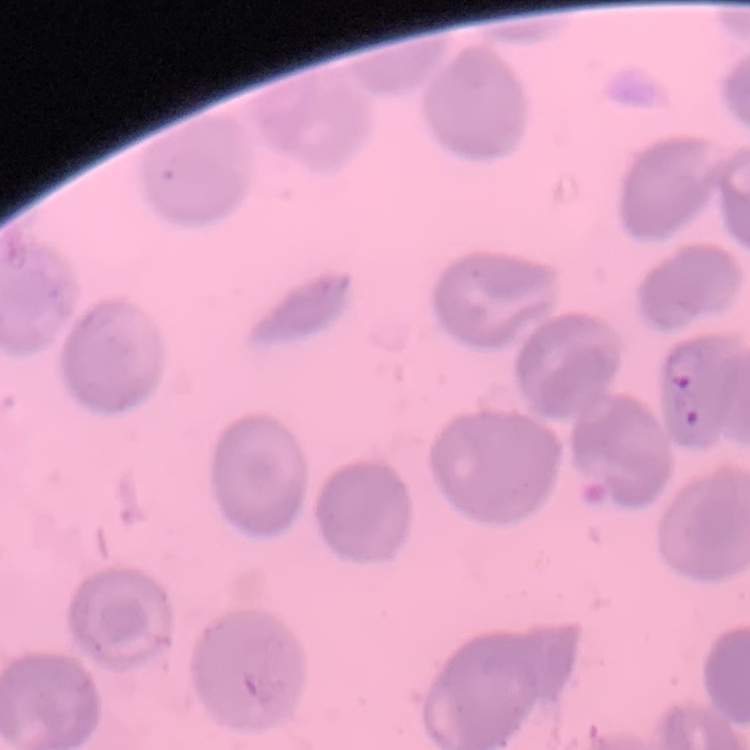
Summary:
  - Red blood cell morphology: no rouleaux formation
  - Preparation: thin blood film
  - Stain: Field's or Giemsa
  - Image type: square crop of a larger photomicrograph